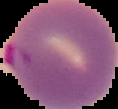
Summary:
  - Preparation: thin blood film
  - Image size: 118×109 pixels
  - Image type: segmented cell region with the area outside set to black
  - Result: malaria parasites identified